Locate every blood parasite and identify its species.
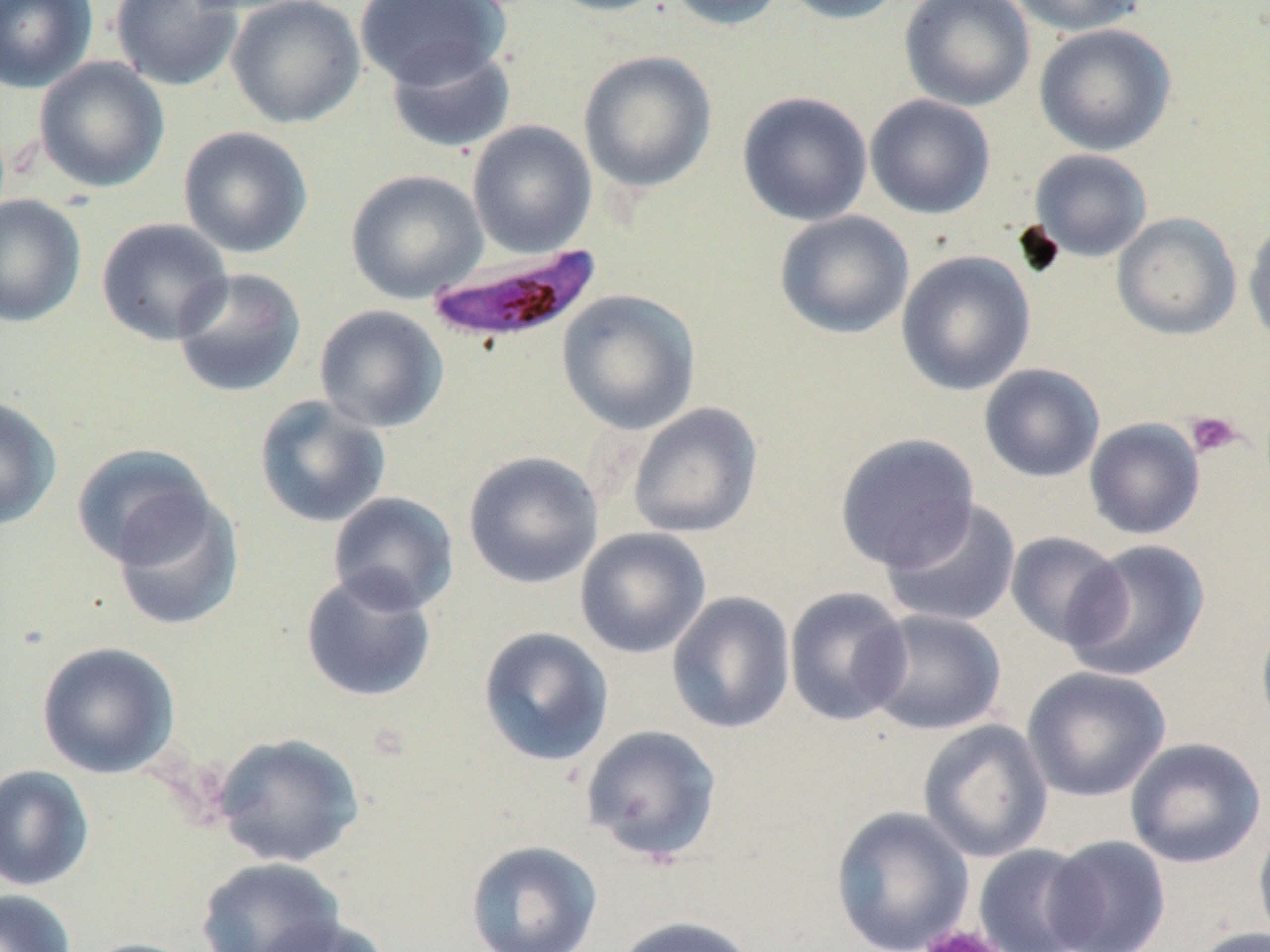
Approximate bounding boxes as named x1/y1/x2/y2 corners in pixels.
Plasmodium falciparum-infected red blood cells: (x1=425, y1=245, x2=602, y2=347).
No Plasmodium ovale, Plasmodium malariae, Plasmodium vivax, Babesia divergens, or Trypanosoma brucei observed.

{
  "slide_level_diagnosis": "Plasmodium falciparum",
  "magnification": "1000x",
  "stain": "May-Grünwald-Giemsa",
  "platelet_locations": "approximate bounding boxes as named x1/y1/x2/y2 corners in pixels: (x1=1184, y1=411, x2=1243, y2=459), (x1=918, y1=924, x2=1008, y2=952)",
  "field_of_view": "one of a larger specimen",
  "image_size": "1270×952 pixels",
  "uninfected_red_blood_cell_locations": "approximate bounding boxes as named x1/y1/x2/y2 corners in pixels: (x1=0, y1=0, x2=97, y2=93), (x1=111, y1=0, x2=243, y2=92), (x1=226, y1=0, x2=365, y2=129), (x1=354, y1=0, x2=509, y2=90), (x1=542, y1=0, x2=678, y2=17), (x1=662, y1=0, x2=788, y2=32), (x1=777, y1=0, x2=908, y2=25), (x1=899, y1=0, x2=1035, y2=112), (x1=1007, y1=0, x2=1147, y2=37), (x1=1034, y1=23, x2=1176, y2=157), (x1=385, y1=43, x2=516, y2=154), (x1=578, y1=50, x2=718, y2=193), (x1=33, y1=57, x2=170, y2=194), (x1=736, y1=91, x2=873, y2=226), (x1=865, y1=94, x2=996, y2=220), (x1=467, y1=120, x2=598, y2=258), (x1=177, y1=126, x2=313, y2=259), (x1=1029, y1=148, x2=1152, y2=262), (x1=345, y1=169, x2=488, y2=304), (x1=0, y1=194, x2=87, y2=328), (x1=774, y1=210, x2=915, y2=339), (x1=1112, y1=212, x2=1242, y2=341), (x1=95, y1=217, x2=234, y2=345), (x1=1243, y1=219, x2=1270, y2=350), (x1=896, y1=250, x2=1036, y2=396), (x1=172, y1=267, x2=308, y2=399), (x1=557, y1=289, x2=701, y2=434), (x1=314, y1=304, x2=449, y2=434), (x1=978, y1=364, x2=1106, y2=483), (x1=253, y1=395, x2=392, y2=529), (x1=0, y1=396, x2=62, y2=531), (x1=627, y1=402, x2=763, y2=539), (x1=1083, y1=418, x2=1206, y2=540), (x1=836, y1=433, x2=979, y2=572), (x1=71, y1=443, x2=216, y2=568), (x1=463, y1=451, x2=604, y2=589), (x1=111, y1=491, x2=244, y2=633), (x1=327, y1=491, x2=460, y2=615), (x1=880, y1=498, x2=1022, y2=630), (x1=574, y1=527, x2=711, y2=659), (x1=1004, y1=531, x2=1128, y2=650), (x1=1064, y1=539, x2=1211, y2=681), (x1=300, y1=568, x2=438, y2=703), (x1=783, y1=587, x2=913, y2=726), (x1=666, y1=591, x2=796, y2=735), (x1=864, y1=608, x2=1006, y2=736), (x1=1255, y1=608, x2=1270, y2=736), (x1=477, y1=626, x2=614, y2=767), (x1=36, y1=641, x2=179, y2=778), (x1=1021, y1=666, x2=1172, y2=802), (x1=918, y1=719, x2=1054, y2=863), (x1=580, y1=724, x2=723, y2=864), (x1=212, y1=732, x2=365, y2=868), (x1=1124, y1=737, x2=1267, y2=869), (x1=0, y1=764, x2=95, y2=891), (x1=829, y1=805, x2=975, y2=952), (x1=1253, y1=818, x2=1270, y2=951), (x1=1043, y1=835, x2=1172, y2=951), (x1=464, y1=839, x2=603, y2=951), (x1=972, y1=844, x2=1100, y2=952), (x1=196, y1=856, x2=346, y2=952), (x1=0, y1=888, x2=78, y2=952), (x1=255, y1=915, x2=392, y2=952), (x1=611, y1=915, x2=762, y2=952), (x1=1185, y1=926, x2=1270, y2=952), (x1=78, y1=937, x2=204, y2=952)",
  "modality": "light microscopy",
  "preparation": "thin blood film"
}